Report the malaria status of this cell.
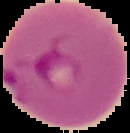
Parasitized.

preparation = thin blood smear
image size = 130×133 pixels
image type = segmented cell region on a black background